Give the extent of all Plasmodium malariae-infected red blood cells.
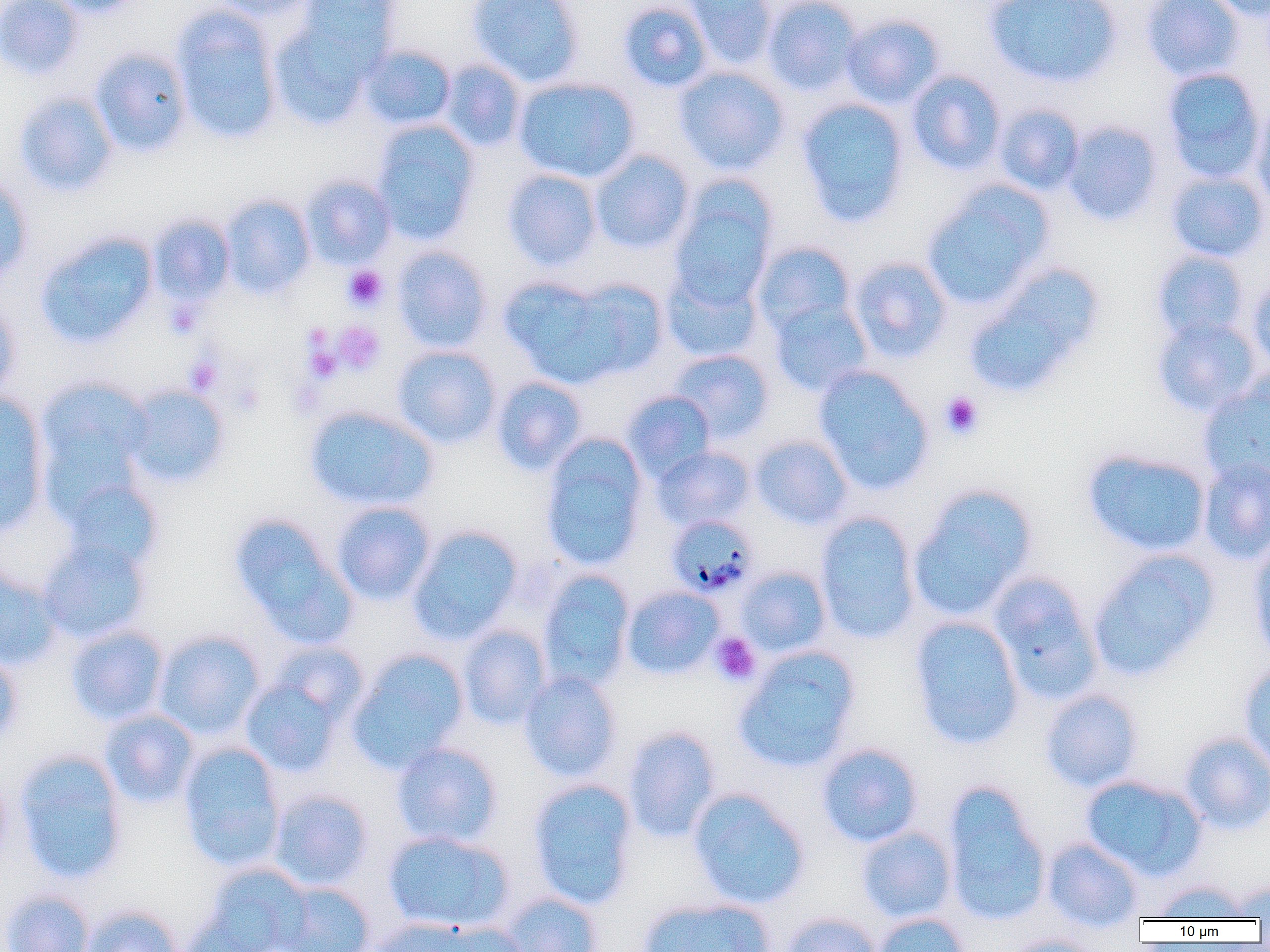
Approximate bounding boxes as (x1,y1)-(x2,y2) corner pairs in pixels.
Plasmodium malariae-infected red blood cells: (666,515)-(759,598).

Summary:
  - Uninfected red blood cell locations: (0,0)-(84,80), (45,0)-(147,17), (211,0)-(320,21), (297,0)-(402,72), (466,0)-(585,87), (681,0)-(778,69), (761,0)-(864,96), (984,0)-(1122,88), (1141,0)-(1245,81), (1206,0)-(1270,21), (618,1)-(713,92), (171,7)-(284,144), (842,13)-(945,108), (268,14)-(379,130), (360,45)-(457,130), (89,47)-(193,156), (439,59)-(527,151), (673,66)-(791,175), (1161,67)-(1266,182), (907,70)-(1007,175), (513,76)-(640,183), (14,91)-(118,196), (796,97)-(911,227), (1251,100)-(1270,213), (994,103)-(1086,195), (371,119)-(481,244), (1062,120)-(1164,226), (589,149)-(695,254), (503,169)-(603,271), (1165,170)-(1269,262), (300,174)-(397,269), (0,175)-(33,282), (669,179)-(777,307), (922,181)-(1053,311), (219,195)-(316,299), (147,214)-(235,305), (35,231)-(158,348), (751,241)-(858,336), (392,246)-(493,352), (1150,249)-(1249,343), (848,256)-(954,362), (965,263)-(1103,396), (660,265)-(765,363), (1246,274)-(1270,376), (499,276)-(618,384), (563,278)-(669,380), (0,299)-(21,402), (768,300)-(873,397), (1152,317)-(1263,417), (392,345)-(502,449), (668,349)-(774,442), (813,365)-(934,494), (491,375)-(588,476), (34,377)-(153,506), (1199,381)-(1270,488), (122,384)-(231,488), (621,390)-(717,482), (0,391)-(51,533), (305,405)-(438,511), (540,434)-(650,571), (750,434)-(853,530), (651,444)-(757,531), (1083,449)-(1211,557), (1198,457)-(1270,564), (60,479)-(164,575), (908,486)-(1037,621), (331,501)-(436,605), (815,512)-(921,643), (229,513)-(355,646), (407,525)-(524,644), (37,539)-(151,644), (1248,540)-(1270,663), (1088,549)-(1219,680), (0,565)-(63,670), (736,565)-(832,657), (537,570)-(635,690), (988,571)-(1103,705), (622,586)-(725,679), (909,615)-(1025,749), (67,625)-(169,725), (457,625)-(553,729), (153,629)-(266,740), (267,641)-(371,727), (733,646)-(861,773), (0,649)-(22,748), (346,649)-(469,772), (1239,662)-(1270,776), (518,671)-(622,782), (240,675)-(346,777), (1040,689)-(1143,791), (100,709)-(200,808), (623,726)-(722,842), (1180,731)-(1270,834), (178,742)-(286,871), (391,742)-(503,848), (816,743)-(924,847), (14,749)-(129,884), (0,773)-(12,871), (1081,774)-(1207,880), (527,777)-(639,909), (942,783)-(1052,926), (688,788)-(810,909), (268,789)-(374,891), (856,826)-(957,923), (383,830)-(515,933), (1042,837)-(1144,928), (202,864)-(313,952), (1151,879)-(1251,920), (1228,881)-(1270,919), (273,882)-(377,952), (1,889)-(95,952), (498,891)-(604,952), (637,896)-(776,952), (80,904)-(185,952), (781,911)-(882,952), (179,913)-(272,952), (872,913)-(971,952), (365,917)-(496,952), (999,934)-(1106,952)
  - Platelet locations: (342,265)-(388,313), (165,299)-(203,338), (333,321)-(385,375), (303,323)-(332,354), (304,344)-(342,382), (185,356)-(224,394), (287,378)-(325,418), (232,382)-(264,416), (940,392)-(985,440), (710,632)-(761,686)
  - Slide-level diagnosis: Plasmodium malariae
  - Magnification: 1000x
  - Modality: light microscopy
  - Image size: 1270×952 pixels
  - Preparation: thin blood film
  - Field of view: one of a larger specimen